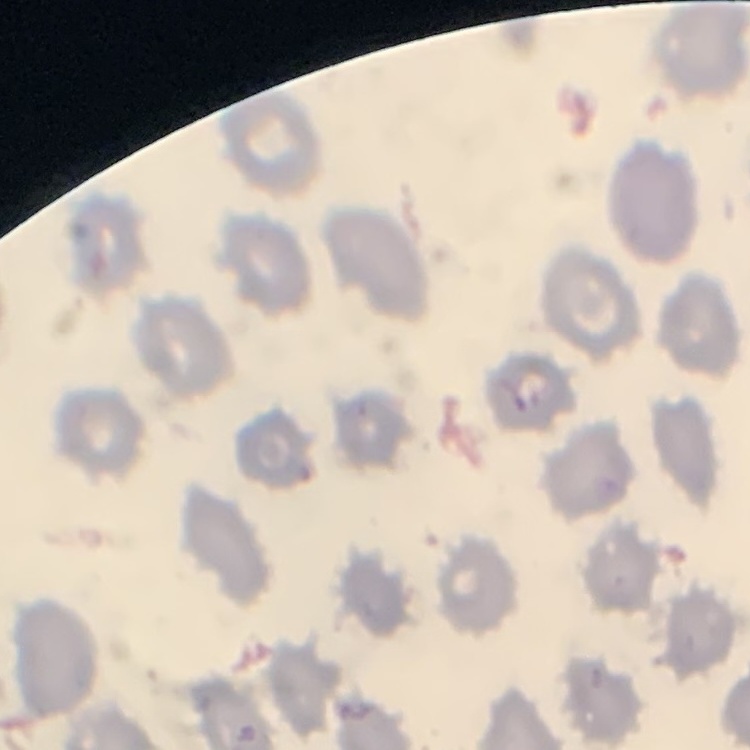

{
  "red_blood_cell_morphology": "no rouleaux formation",
  "image_type": "square crop of a larger photomicrograph",
  "stain": "Field's or Giemsa",
  "preparation": "thin blood film"
}